Report the malaria status of this cell.
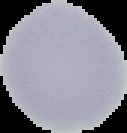
Uninfected.

Segmented cell region on a black background. Image is 127×133 pixels. From a thin blood smear.